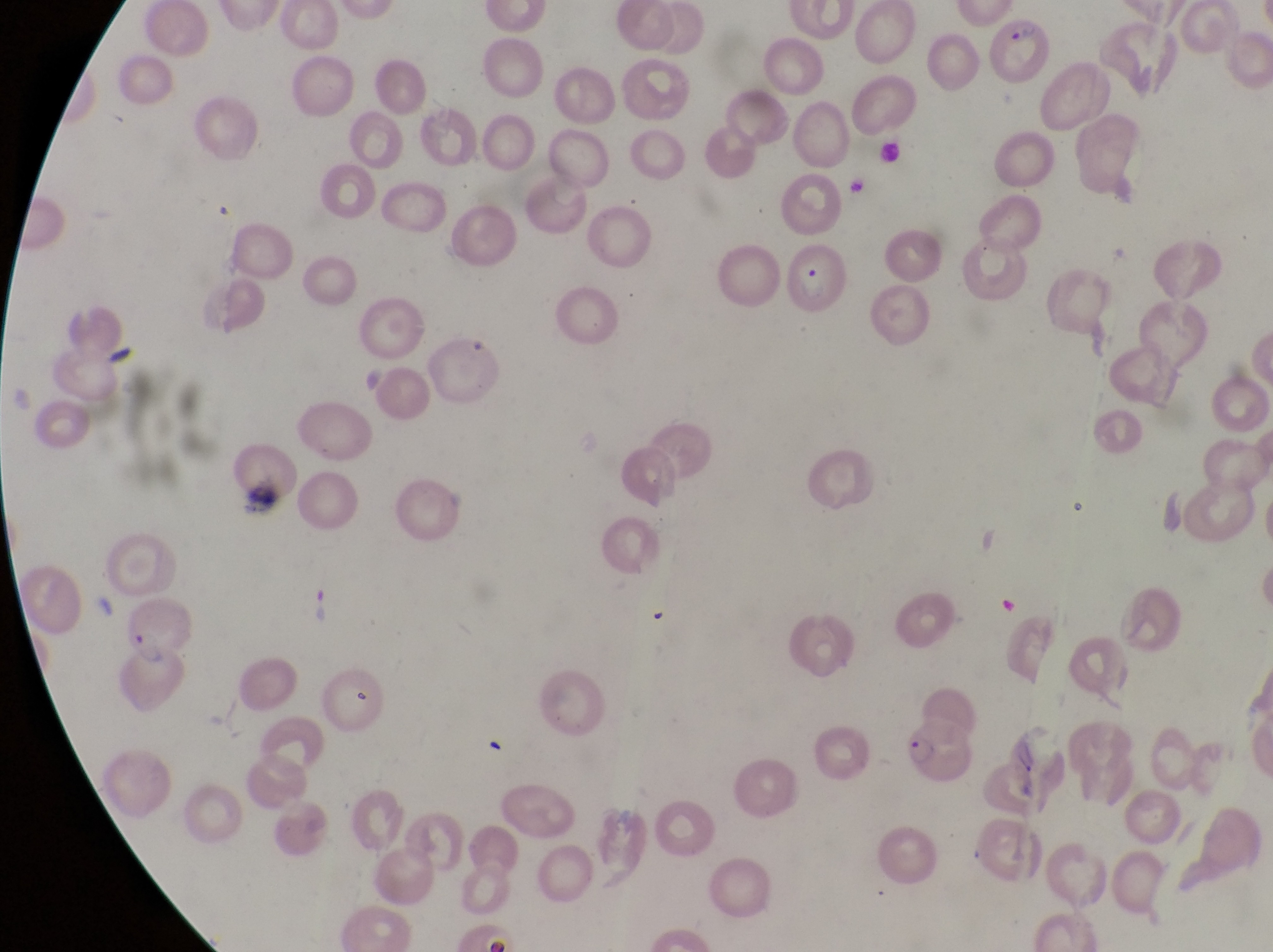
{
  "image_size": "1273×952 pixels",
  "artifact_platelet_like_body_stain_precipitate_or_debris_locations": "approximate bounding boxes as {left, top, right, bottom} in pixels: {244, 481, 282, 524}",
  "country": "Uganda",
  "magnification": "1000x",
  "preparation": "thin blood smear",
  "parasitised_red_blood_cell_locations": "approximate bounding boxes as {left, top, right, bottom} in pixels: {993, 13, 1046, 78}, {784, 242, 849, 319}, {120, 600, 200, 728}, {909, 717, 979, 795}",
  "field_of_view": "single",
  "capture": "smartphone photograph through the eyepiece of an Olympus CX-23 microscope"
}